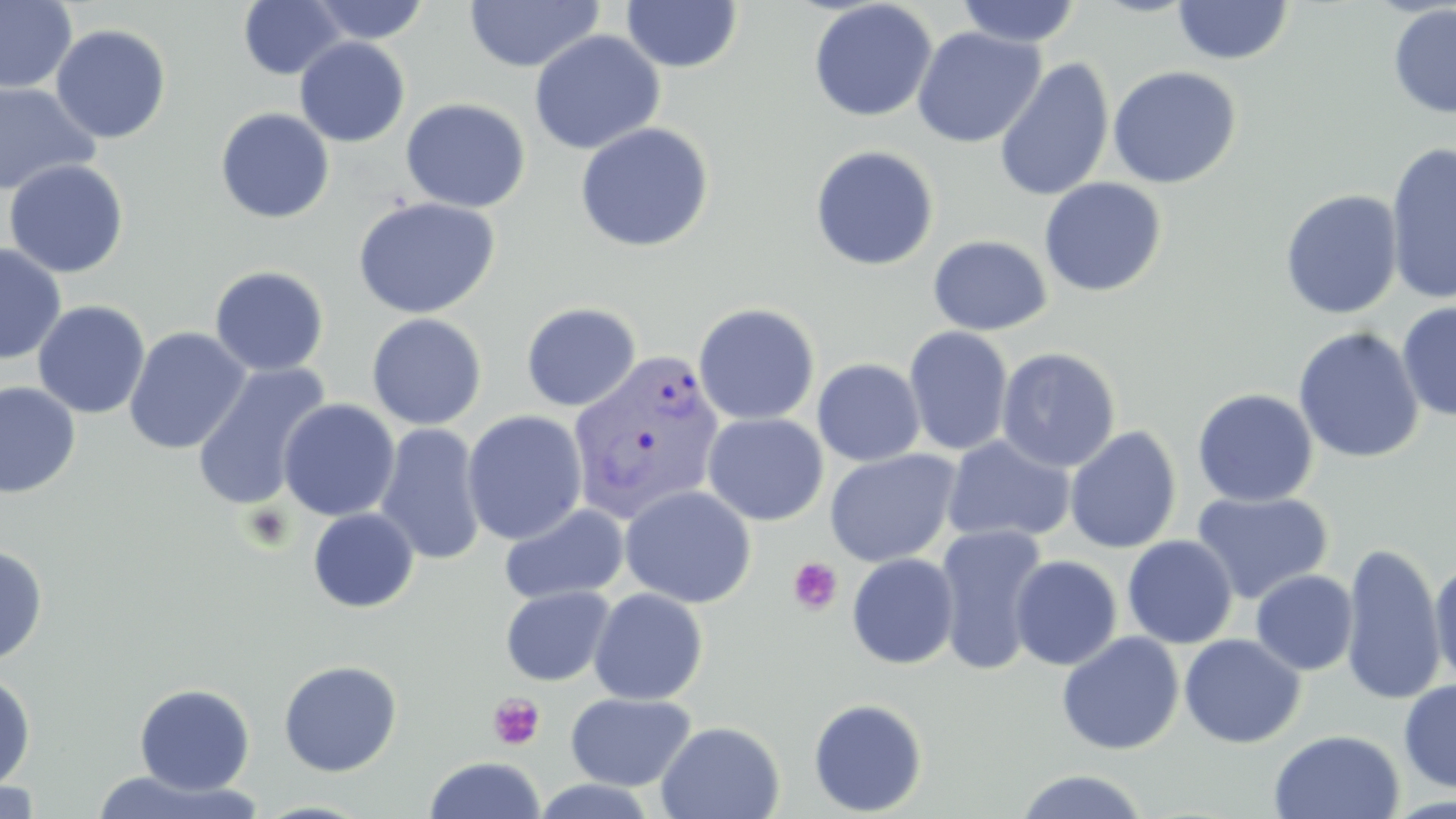

Summary:
  - Coordinate format: approximate bounding boxes as [x1, y1, x2, y2] in pixels
  - Uninfected red blood cell locations: [238, 0, 347, 80], [307, 0, 431, 45], [463, 0, 604, 73], [619, 0, 744, 73], [955, 0, 1082, 48], [0, 1, 77, 95], [808, 1, 938, 123], [1171, 1, 1295, 65], [1387, 4, 1456, 119], [50, 24, 172, 143], [911, 26, 1046, 149], [528, 30, 666, 155], [294, 37, 410, 147], [994, 57, 1115, 202], [1106, 65, 1242, 189], [0, 81, 101, 197], [400, 97, 531, 213], [215, 107, 335, 224], [574, 121, 714, 253], [1385, 141, 1456, 307], [809, 144, 940, 271], [3, 159, 130, 278], [1039, 177, 1167, 298], [1279, 188, 1404, 319], [351, 197, 501, 320], [927, 235, 1053, 336], [0, 243, 67, 364], [209, 265, 330, 377], [32, 300, 151, 419], [1396, 300, 1456, 421], [521, 302, 642, 412], [692, 302, 821, 425], [366, 313, 487, 430], [903, 326, 1014, 456], [1292, 326, 1425, 464], [123, 327, 250, 455], [996, 347, 1120, 473], [812, 358, 926, 466], [191, 362, 331, 512], [0, 381, 81, 499], [1192, 388, 1318, 507], [278, 399, 400, 522], [462, 410, 588, 545], [702, 413, 828, 526], [375, 423, 487, 566], [1065, 426, 1182, 554], [942, 435, 1076, 544], [824, 449, 962, 568], [619, 484, 757, 608], [1191, 491, 1333, 604], [499, 503, 629, 605], [307, 507, 420, 613], [935, 523, 1050, 676], [1122, 535, 1238, 649], [1340, 542, 1446, 704], [0, 544, 49, 665], [846, 552, 959, 669], [1009, 555, 1122, 671], [1430, 557, 1456, 690], [1250, 570, 1358, 675], [500, 586, 615, 686], [589, 587, 708, 705], [1056, 631, 1184, 755], [1179, 633, 1306, 749], [278, 659, 403, 777], [0, 671, 37, 793], [1398, 678, 1456, 793], [134, 683, 255, 795], [565, 692, 697, 791], [808, 697, 928, 816], [656, 720, 785, 819], [1269, 729, 1405, 818], [423, 756, 547, 819], [87, 769, 263, 818], [1013, 769, 1152, 819], [0, 779, 42, 818], [528, 779, 662, 818], [252, 799, 376, 818]
  - Plasmodium vivax-infected red blood cell locations: [566, 349, 725, 524]
  - Platelet locations: [243, 503, 294, 551], [788, 557, 843, 615], [487, 692, 546, 751]
  - Slide-level diagnosis: Plasmodium vivax
  - Image size: 1456×819 pixels
  - Field of view: single
  - Modality: optical microscopy
  - Stain: May-Grünwald-Giemsa
  - Magnification: 1000x
  - Preparation: thin blood film